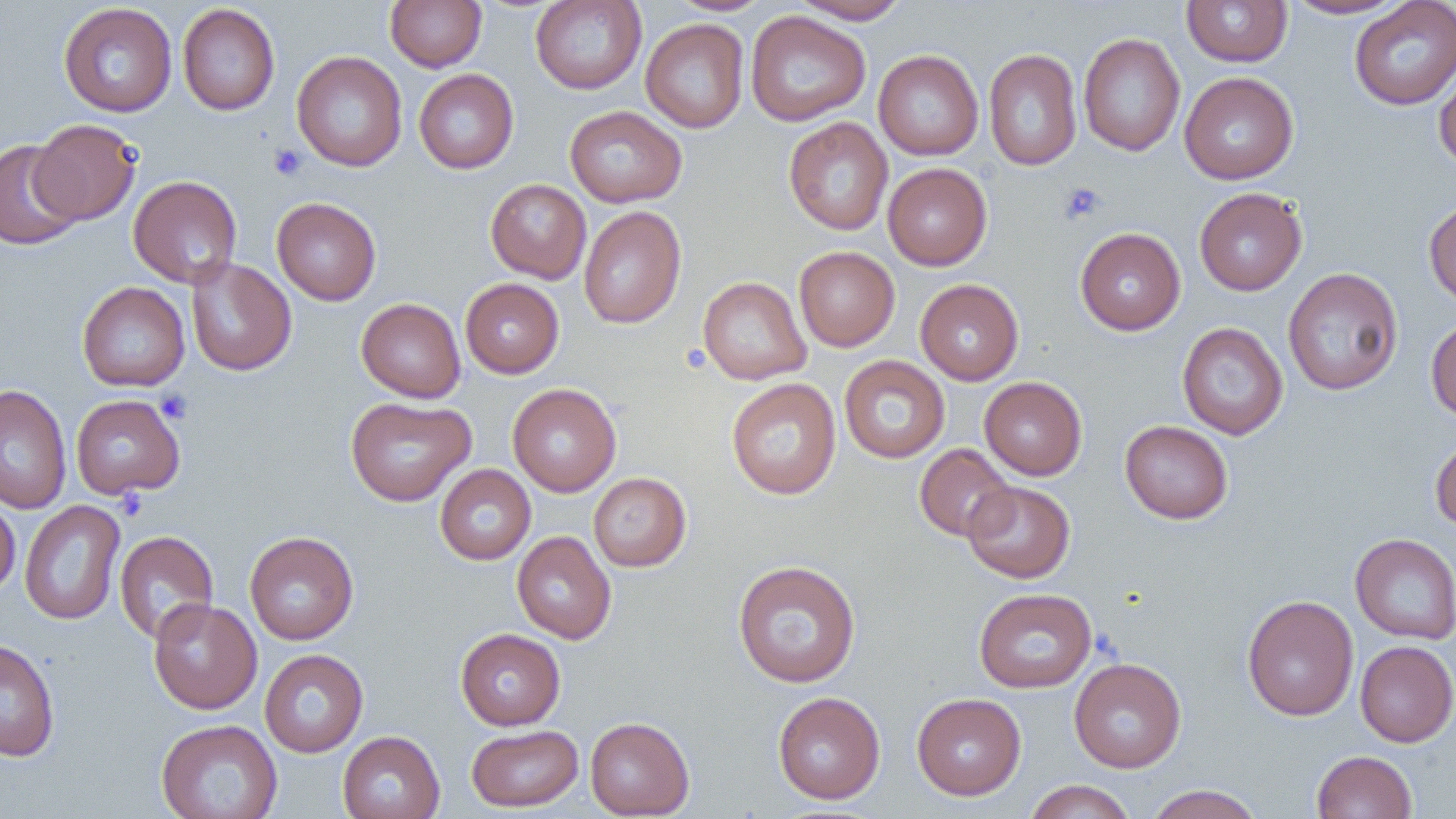

Summary:
  - Coordinate format: approximate bounding boxes as named x1/y1/x2/y2 corners in pixels
  - Uninfected red blood cell locations: (x1=385, y1=0, x2=487, y2=72), (x1=530, y1=0, x2=647, y2=94), (x1=667, y1=0, x2=775, y2=16), (x1=1181, y1=0, x2=1292, y2=67), (x1=1284, y1=0, x2=1410, y2=20), (x1=791, y1=1, x2=912, y2=25), (x1=1349, y1=1, x2=1456, y2=110), (x1=58, y1=3, x2=177, y2=118), (x1=177, y1=3, x2=280, y2=115), (x1=745, y1=11, x2=871, y2=127), (x1=640, y1=18, x2=749, y2=133), (x1=1078, y1=33, x2=1185, y2=156), (x1=983, y1=48, x2=1082, y2=171), (x1=873, y1=50, x2=983, y2=160), (x1=292, y1=51, x2=407, y2=171), (x1=1434, y1=60, x2=1456, y2=171), (x1=413, y1=69, x2=519, y2=174), (x1=1179, y1=71, x2=1299, y2=184), (x1=564, y1=105, x2=687, y2=207), (x1=783, y1=117, x2=894, y2=235), (x1=29, y1=119, x2=141, y2=225), (x1=0, y1=139, x2=83, y2=250), (x1=883, y1=162, x2=992, y2=270), (x1=128, y1=175, x2=242, y2=288), (x1=485, y1=179, x2=591, y2=284), (x1=1194, y1=187, x2=1307, y2=296), (x1=271, y1=197, x2=381, y2=305), (x1=1423, y1=199, x2=1456, y2=307), (x1=578, y1=206, x2=686, y2=329), (x1=1075, y1=227, x2=1186, y2=335), (x1=794, y1=246, x2=900, y2=352), (x1=185, y1=257, x2=297, y2=376), (x1=1283, y1=267, x2=1403, y2=395), (x1=697, y1=276, x2=812, y2=385), (x1=460, y1=278, x2=564, y2=378), (x1=915, y1=279, x2=1024, y2=385), (x1=77, y1=281, x2=190, y2=391), (x1=356, y1=297, x2=466, y2=403), (x1=1425, y1=316, x2=1456, y2=420), (x1=1177, y1=322, x2=1288, y2=440), (x1=839, y1=355, x2=950, y2=463), (x1=979, y1=376, x2=1087, y2=480), (x1=726, y1=378, x2=841, y2=499), (x1=507, y1=383, x2=621, y2=496), (x1=0, y1=384, x2=72, y2=513), (x1=70, y1=394, x2=186, y2=498), (x1=345, y1=396, x2=476, y2=507), (x1=1119, y1=420, x2=1233, y2=524), (x1=1430, y1=433, x2=1456, y2=531), (x1=914, y1=444, x2=1016, y2=542), (x1=434, y1=464, x2=536, y2=565), (x1=588, y1=472, x2=691, y2=572), (x1=963, y1=480, x2=1075, y2=583), (x1=0, y1=498, x2=20, y2=597), (x1=19, y1=500, x2=126, y2=625), (x1=114, y1=530, x2=219, y2=645), (x1=244, y1=531, x2=359, y2=645), (x1=512, y1=531, x2=616, y2=645), (x1=1350, y1=533, x2=1456, y2=644), (x1=732, y1=560, x2=861, y2=688), (x1=973, y1=587, x2=1097, y2=693), (x1=1242, y1=594, x2=1359, y2=722), (x1=148, y1=598, x2=262, y2=714), (x1=455, y1=627, x2=565, y2=730), (x1=0, y1=638, x2=60, y2=761), (x1=1355, y1=640, x2=1456, y2=747), (x1=259, y1=649, x2=368, y2=758), (x1=1068, y1=657, x2=1186, y2=772), (x1=772, y1=692, x2=885, y2=804), (x1=912, y1=693, x2=1026, y2=800), (x1=585, y1=716, x2=695, y2=818), (x1=156, y1=719, x2=282, y2=819), (x1=466, y1=724, x2=584, y2=812), (x1=337, y1=730, x2=446, y2=819), (x1=1311, y1=750, x2=1418, y2=819), (x1=1023, y1=780, x2=1138, y2=819), (x1=1144, y1=784, x2=1264, y2=819)
  - Platelet locations: (x1=268, y1=143, x2=307, y2=180), (x1=1058, y1=182, x2=1105, y2=225), (x1=155, y1=389, x2=193, y2=424)
  - Slide-level diagnosis: no evidence of blood parasites
  - Modality: light microscopy
  - Image size: 1456×819 pixels
  - Preparation: thin blood smear
  - Field of view: one of a larger specimen
  - Magnification: 1000x